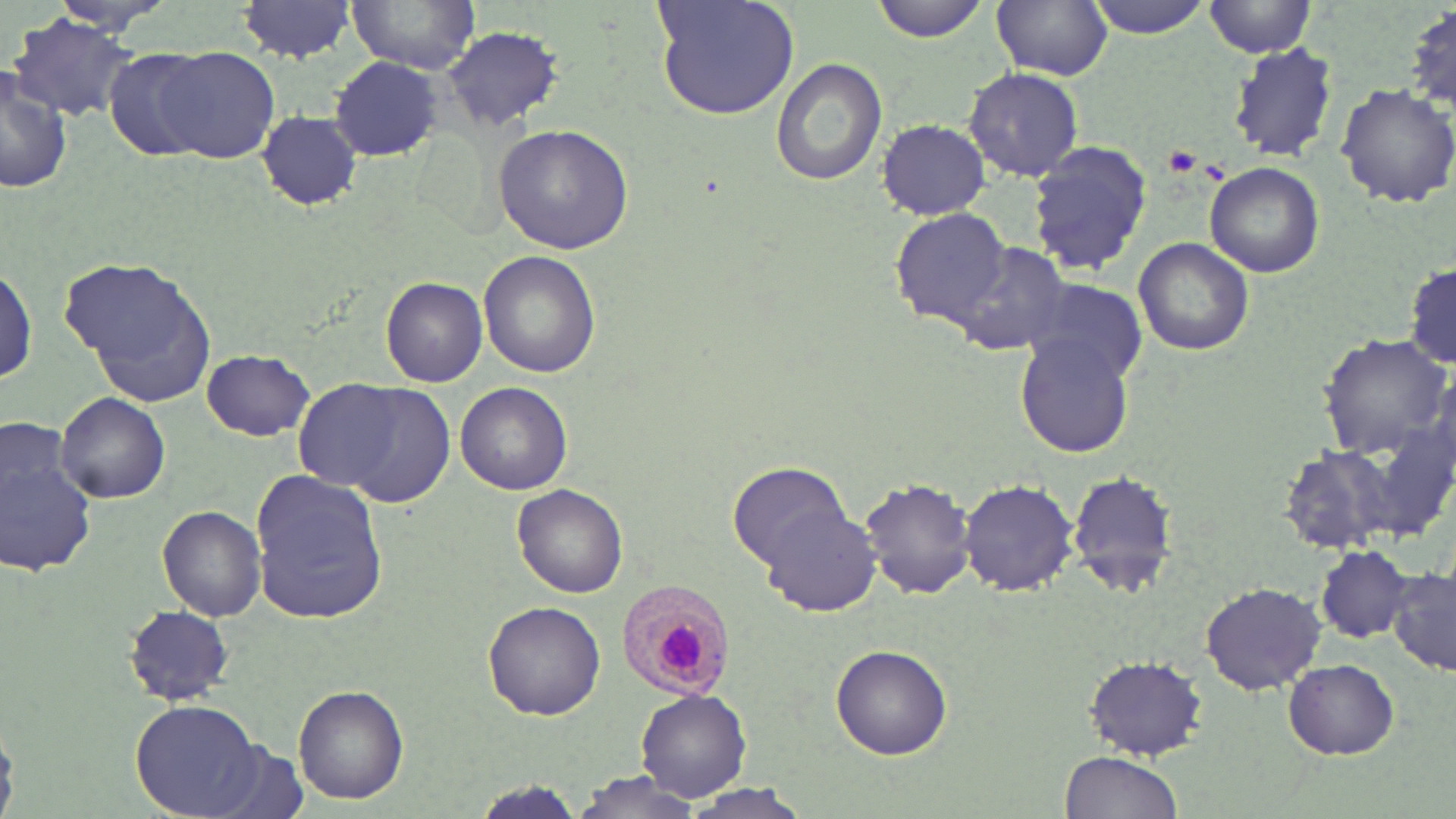

Approximate bounding boxes as (x1,y1)-(x2,y2) corner pairs in pixels. Uninfected red blood cell locations: (235,0)-(361,62), (348,0)-(482,72), (653,0)-(802,122), (870,0)-(992,43), (992,1)-(1110,81), (1078,1)-(1217,36), (1201,1)-(1320,57), (1403,3)-(1456,118), (9,14)-(144,120), (440,27)-(563,131), (1227,42)-(1340,163), (102,46)-(221,162), (161,46)-(280,164), (771,57)-(887,185), (329,58)-(442,162), (1,66)-(73,196), (963,67)-(1086,181), (1335,83)-(1456,210), (257,110)-(363,211), (877,119)-(991,219), (493,124)-(635,253), (1026,139)-(1154,277), (1206,162)-(1326,278), (891,209)-(1014,329), (1133,236)-(1254,356), (951,241)-(1070,356), (479,250)-(599,378), (62,257)-(213,387), (1404,257)-(1456,371), (1,263)-(37,390), (380,277)-(488,387), (1022,281)-(1148,385), (1014,332)-(1135,458), (1318,335)-(1451,459), (201,349)-(314,441), (303,377)-(455,504), (456,383)-(571,496), (56,391)-(170,503), (1279,444)-(1398,557), (0,449)-(96,577), (729,462)-(852,568), (1066,468)-(1180,596), (248,469)-(391,625), (860,476)-(977,601), (959,477)-(1082,596), (514,484)-(629,599), (762,503)-(882,618), (157,505)-(267,620), (1316,546)-(1414,643), (1389,567)-(1455,677), (1200,581)-(1327,695), (482,601)-(605,719), (124,604)-(233,705), (831,644)-(952,759), (1082,656)-(1208,758), (1285,658)-(1401,759), (293,684)-(410,805), (636,689)-(752,803), (131,700)-(265,817), (0,722)-(24,817), (1059,751)-(1184,819), (568,773)-(710,818), (469,782)-(587,815), (683,782)-(814,817). Plasmodium malariae-infected red blood cell locations: (612,580)-(739,703). Platelet locations: (1162,145)-(1203,173). Slide-level diagnosis: Plasmodium malariae. May-Grünwald-Giemsa-stained preparation. Thin blood smear. Image is 1456×819 pixels. Optical microscopy. Single field of view. Captured at 1000x magnification.